Identify the blood parasite species.
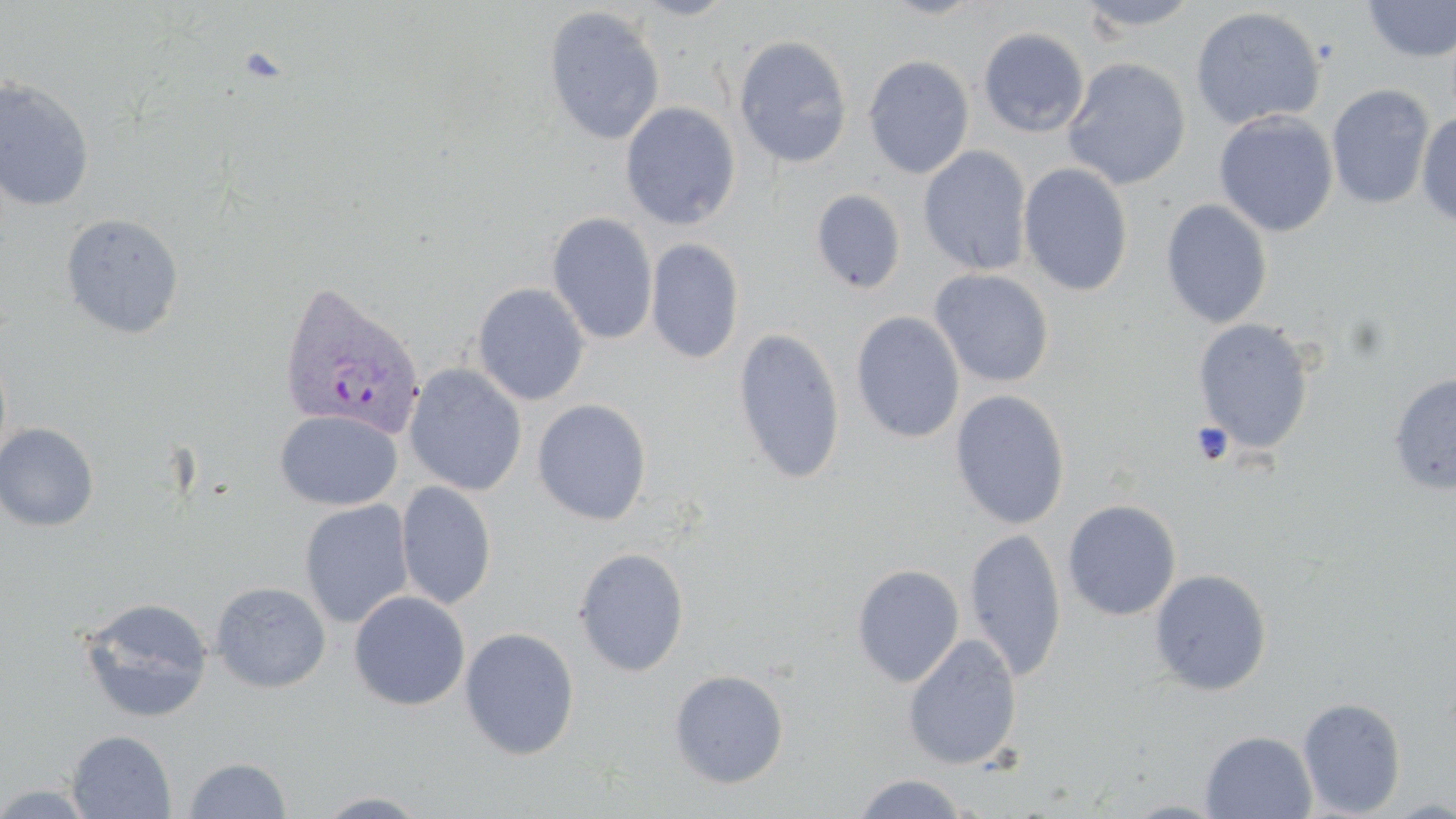
Plasmodium vivax.

Approximate bounding boxes as named x1/y1/x2/y2 corners in pixels. Uninfected red blood cell locations: (x1=630, y1=0, x2=740, y2=20), (x1=876, y1=0, x2=987, y2=20), (x1=1073, y1=0, x2=1205, y2=34), (x1=1360, y1=0, x2=1456, y2=64), (x1=543, y1=6, x2=666, y2=146), (x1=1190, y1=6, x2=1326, y2=131), (x1=979, y1=27, x2=1090, y2=137), (x1=733, y1=35, x2=853, y2=169), (x1=863, y1=55, x2=974, y2=178), (x1=1063, y1=57, x2=1191, y2=190), (x1=0, y1=75, x2=96, y2=211), (x1=1326, y1=84, x2=1434, y2=210), (x1=620, y1=102, x2=741, y2=230), (x1=1213, y1=111, x2=1338, y2=237), (x1=1416, y1=112, x2=1456, y2=228), (x1=918, y1=146, x2=1032, y2=276), (x1=1018, y1=162, x2=1134, y2=297), (x1=811, y1=189, x2=907, y2=294), (x1=1160, y1=199, x2=1273, y2=329), (x1=547, y1=212, x2=658, y2=346), (x1=59, y1=213, x2=185, y2=340), (x1=646, y1=238, x2=744, y2=364), (x1=929, y1=268, x2=1055, y2=387), (x1=473, y1=283, x2=590, y2=406), (x1=851, y1=311, x2=965, y2=444), (x1=1191, y1=318, x2=1316, y2=456), (x1=733, y1=324, x2=968, y2=465), (x1=732, y1=327, x2=846, y2=485), (x1=405, y1=364, x2=527, y2=497), (x1=1388, y1=371, x2=1456, y2=495), (x1=949, y1=389, x2=1070, y2=530), (x1=532, y1=399, x2=652, y2=525), (x1=274, y1=410, x2=402, y2=510), (x1=0, y1=423, x2=100, y2=532), (x1=396, y1=481, x2=497, y2=610), (x1=299, y1=499, x2=414, y2=629), (x1=1062, y1=499, x2=1181, y2=621), (x1=965, y1=528, x2=1066, y2=682), (x1=573, y1=547, x2=689, y2=677), (x1=851, y1=564, x2=965, y2=687), (x1=1149, y1=568, x2=1272, y2=696), (x1=210, y1=581, x2=331, y2=693), (x1=349, y1=590, x2=471, y2=711), (x1=77, y1=596, x2=213, y2=724), (x1=459, y1=627, x2=580, y2=761), (x1=903, y1=632, x2=1022, y2=771), (x1=668, y1=669, x2=789, y2=789), (x1=1297, y1=697, x2=1406, y2=817), (x1=67, y1=730, x2=176, y2=818), (x1=1200, y1=731, x2=1317, y2=819), (x1=182, y1=756, x2=292, y2=818), (x1=851, y1=773, x2=973, y2=818), (x1=0, y1=782, x2=100, y2=818), (x1=312, y1=791, x2=433, y2=818). Platelet locations: (x1=1189, y1=421, x2=1234, y2=466). Plasmodium vivax-infected red blood cell locations: (x1=277, y1=281, x2=426, y2=441). 1000x magnification. One field of a larger specimen. May-Grünwald-Giemsa stain. Thin blood smear. Image is 1456×819 pixels. Optical microscopy.